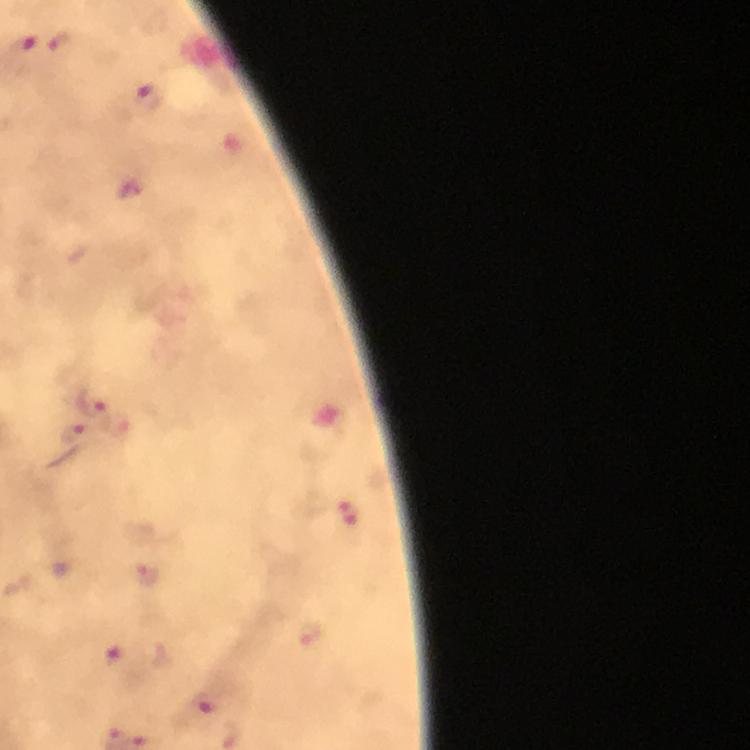
context = from a malaria diagnostic workup
immersion oil = used
image size = 750×750 pixels
preparation = thick blood film
magnification = 100x
cropped from = a single field of view
malaria parasite locations = approximate centers as (x, y) in pixels: (61, 43), (21, 48), (147, 97), (130, 191), (91, 401), (74, 434), (345, 517), (149, 578), (119, 652), (204, 705)
capture = smartphone mounted on the microscope
stain = Giemsa